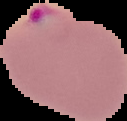 Image is 127×121 pixels. From a thin blood smear. Malaria status: parasitized. Segmented cell region on a black background.